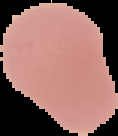
Summary:
  - Image size: 118×136 pixels
  - Preparation: thin blood smear
  - Image type: segmented cell region on a black background
  - Result: no Plasmodium parasites seen